Assess this cell for malaria.
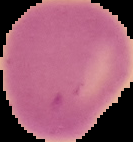

It is uninfected.

The area outside the segmented cell region is set to black. From a thin blood smear. Image is 133×142 pixels.